Name the parasite shown.
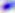
This is Toxoplasma gondii.

Summary:
  - Magnification: 400x
  - Modality: photomicrograph